Comment on the morphology of the red blood cells.
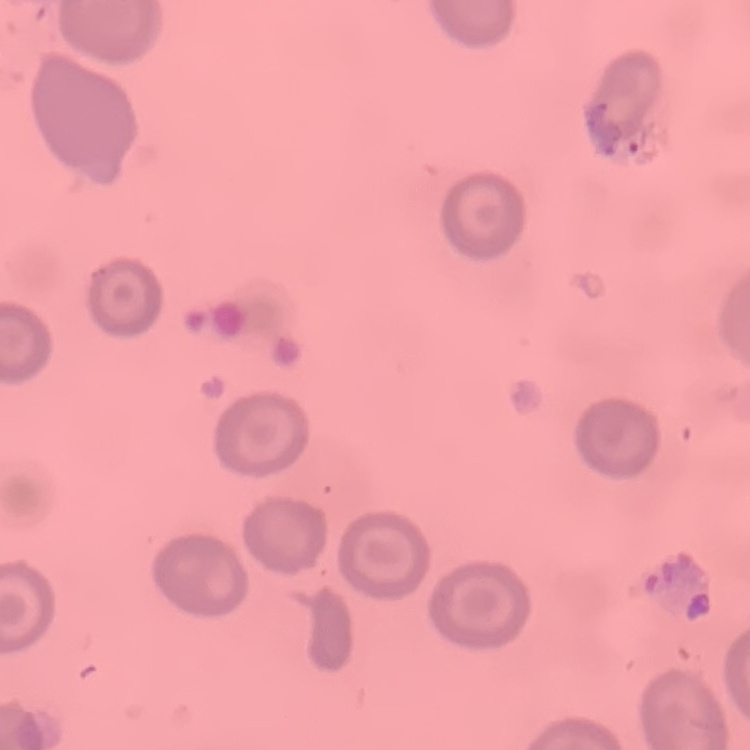

They show no rouleaux formation.

Summary:
  - Image type: one tile cut from a larger photomicrograph
  - Preparation: thin blood film
  - Stain: Field's or Giemsa